Outline each blood parasite and name the species.
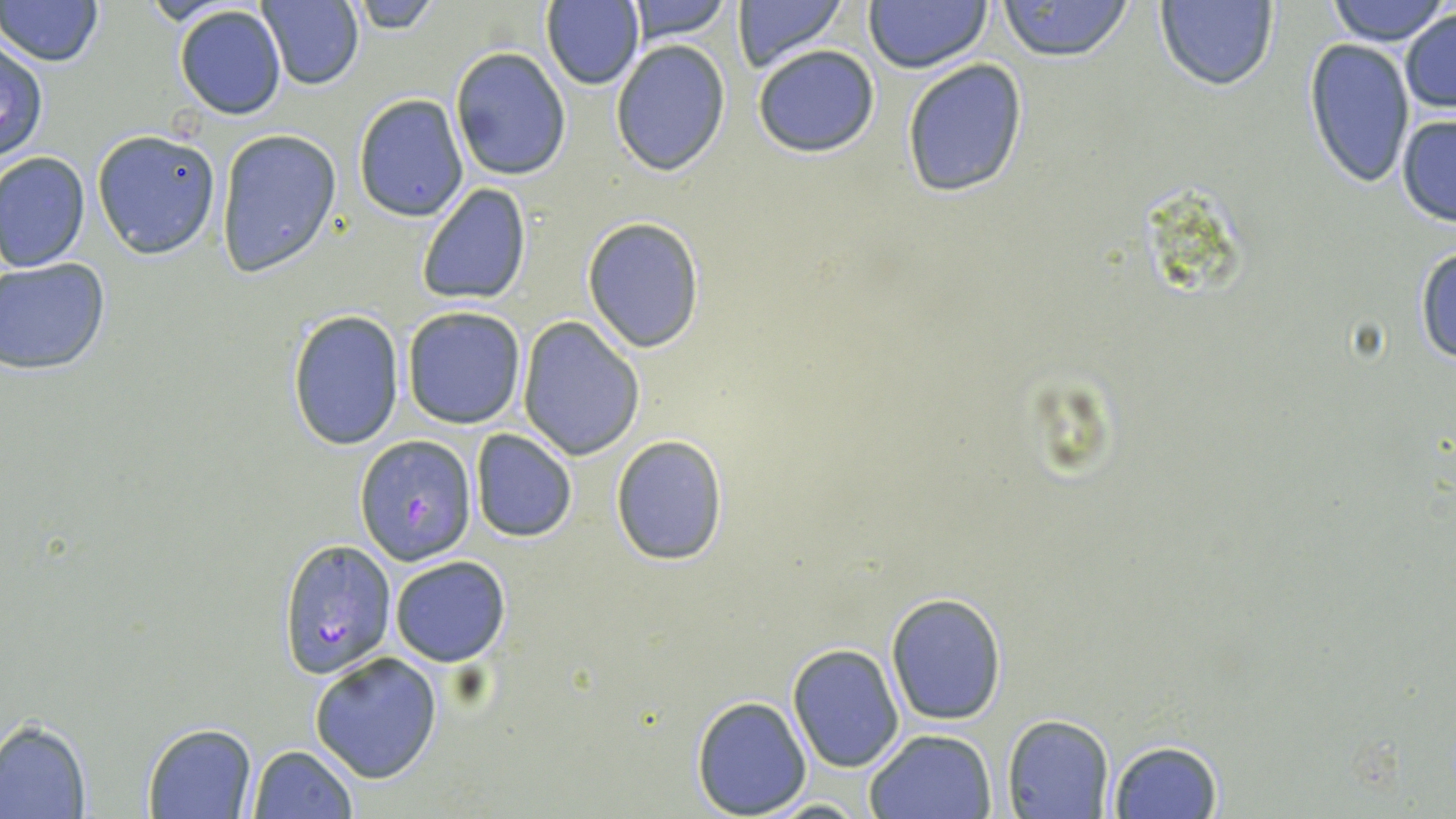

Approximate bounding boxes as (x1, y1, x2, y2) in pixels.
Plasmodium falciparum-infected red blood cells: (356, 436, 477, 564), (279, 540, 397, 676).
No Plasmodium ovale, Plasmodium malariae, Plasmodium vivax, Babesia divergens, or Trypanosoma brucei observed.

Uninfected red blood cell locations: (1, 0, 103, 68), (347, 0, 443, 34), (619, 0, 734, 44), (732, 0, 848, 71), (865, 0, 990, 73), (998, 0, 1134, 63), (1326, 0, 1449, 47), (256, 1, 365, 89), (541, 1, 646, 91), (1155, 1, 1279, 89), (173, 6, 287, 119), (1399, 9, 1456, 114), (0, 37, 49, 163), (1304, 38, 1414, 187), (610, 39, 731, 177), (752, 44, 881, 158), (449, 45, 572, 181), (899, 59, 1030, 199), (353, 94, 468, 221), (1397, 114, 1456, 228), (93, 128, 222, 259), (216, 128, 342, 277), (0, 152, 90, 273), (416, 183, 533, 307), (582, 217, 706, 353), (1414, 246, 1456, 365), (0, 257, 113, 376), (401, 306, 527, 429), (287, 309, 406, 450), (516, 318, 645, 460), (469, 429, 577, 542), (608, 434, 730, 565), (388, 555, 511, 667), (884, 592, 1007, 726), (787, 643, 904, 772), (308, 652, 443, 783), (691, 694, 812, 817), (1003, 714, 1113, 819), (0, 720, 92, 818), (141, 722, 257, 818), (864, 728, 997, 818), (1106, 739, 1224, 818), (247, 744, 358, 818), (761, 797, 872, 816). Slide-level diagnosis: Plasmodium falciparum. Single field of view. May-Grünwald-Giemsa stain. 1000x magnification. Thin blood smear. Light microscopy. Image is 1456×819 pixels.